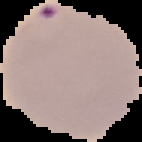
Malaria status: parasitized. Cell region segmented out of the field of view; the surrounding area is masked to black. From a thin blood smear. Image is 142×142 pixels.